Report the malaria status of this cell.
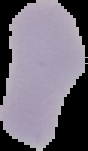

Uninfected.

{
  "preparation": "thin blood smear",
  "image_size": "88×151 pixels",
  "image_type": "cell region segmented out of the field of view; surrounding area masked to black"
}